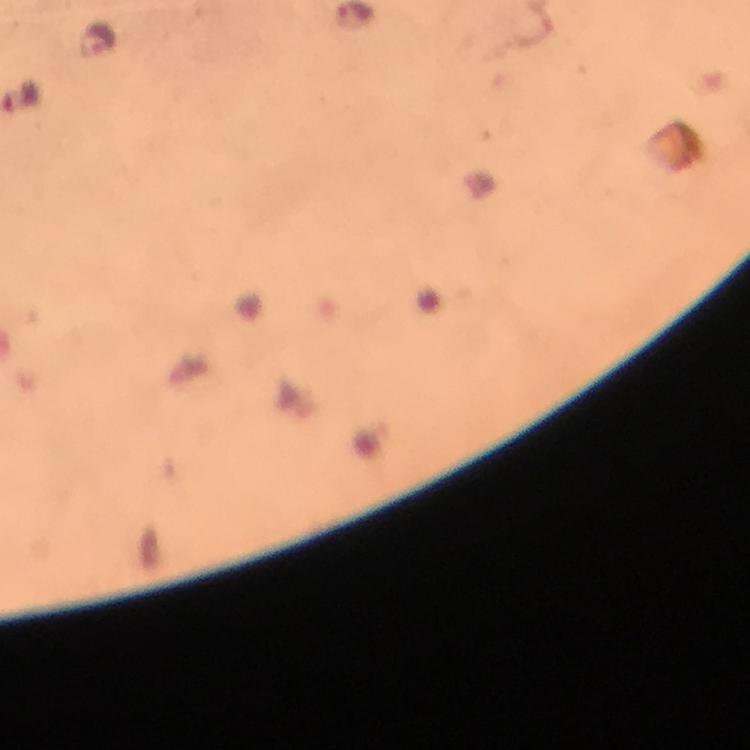
Approximate centers as {x, y} in pixels. Plasmodium parasite locations: {99, 39}. Immersion oil applied. Thick blood smear. 100x magnification. Giemsa-stained preparation. Image is 750×750 pixels. From a malaria diagnostic workup. Photographed through the microscope with a smartphone camera. Cropped region of a single field of view.